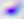
400x magnification. Photomicrograph. Toxoplasma gondii is shown.